Name the cell type shown.
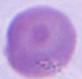

An erythrocyte.

Photomicrograph. 1000x magnification.